Assess this cell for malaria.
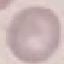

It is uninfected.

Summary:
  - Stain: Giemsa
  - Image type: cell patch, automatically extracted from a larger field of view and resized to 64 × 64 pixels
  - Preparation: thin blood smear
  - Capture: smartphone camera at the microscope eyepiece